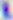 Captured at 400x magnification. Photomicrograph. Toxoplasma gondii is shown.